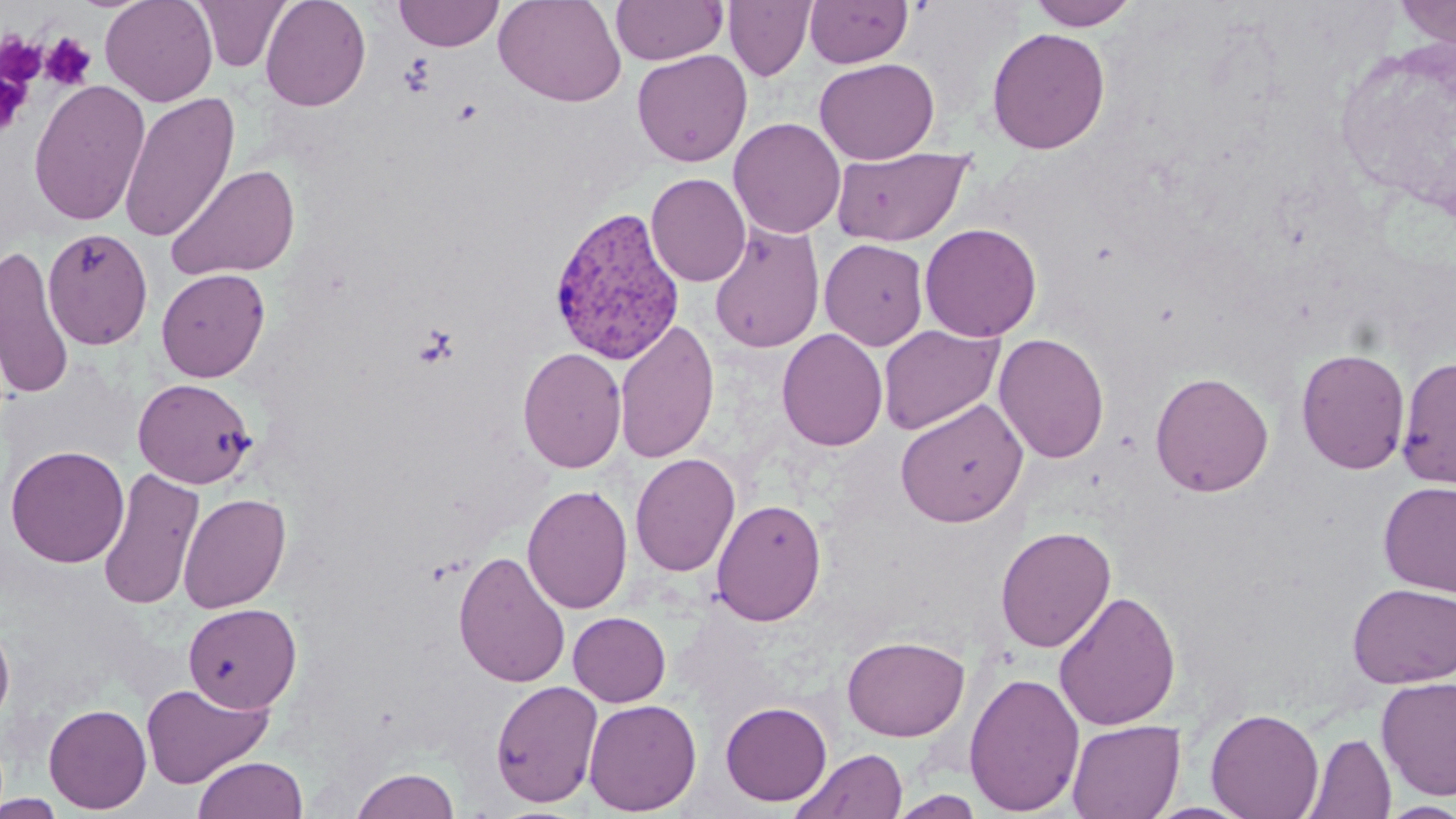
Summary:
  - Coordinate format: approximate bounding boxes as named x1/y1/x2/y2 corners in pixels
  - Platelet locations: (x1=0, y1=33, x2=46, y2=88), (x1=40, y1=33, x2=97, y2=91), (x1=0, y1=71, x2=31, y2=138)
  - Uninfected red blood cell locations: (x1=100, y1=0, x2=218, y2=107), (x1=192, y1=0, x2=290, y2=72), (x1=260, y1=0, x2=371, y2=111), (x1=393, y1=0, x2=505, y2=51), (x1=494, y1=0, x2=627, y2=107), (x1=610, y1=0, x2=727, y2=65), (x1=804, y1=0, x2=913, y2=68), (x1=1025, y1=0, x2=1141, y2=30), (x1=1392, y1=0, x2=1456, y2=47), (x1=723, y1=1, x2=816, y2=81), (x1=986, y1=27, x2=1111, y2=154), (x1=632, y1=49, x2=752, y2=167), (x1=814, y1=58, x2=939, y2=164), (x1=28, y1=79, x2=151, y2=227), (x1=119, y1=91, x2=239, y2=243), (x1=728, y1=117, x2=846, y2=239), (x1=831, y1=146, x2=972, y2=247), (x1=164, y1=163, x2=300, y2=282), (x1=645, y1=173, x2=751, y2=286), (x1=708, y1=222, x2=825, y2=353), (x1=919, y1=223, x2=1042, y2=341), (x1=42, y1=227, x2=153, y2=349), (x1=819, y1=238, x2=929, y2=351), (x1=0, y1=243, x2=75, y2=401), (x1=156, y1=268, x2=270, y2=381), (x1=614, y1=319, x2=719, y2=464), (x1=878, y1=324, x2=1004, y2=435), (x1=777, y1=328, x2=888, y2=451), (x1=993, y1=333, x2=1110, y2=464), (x1=517, y1=347, x2=627, y2=473), (x1=1296, y1=348, x2=1411, y2=474), (x1=1396, y1=356, x2=1456, y2=489), (x1=1150, y1=371, x2=1274, y2=497), (x1=133, y1=378, x2=256, y2=488), (x1=895, y1=398, x2=1028, y2=527), (x1=6, y1=444, x2=129, y2=568), (x1=629, y1=453, x2=740, y2=577), (x1=97, y1=467, x2=204, y2=610), (x1=1378, y1=481, x2=1456, y2=596), (x1=522, y1=484, x2=633, y2=615), (x1=177, y1=492, x2=291, y2=613), (x1=711, y1=498, x2=827, y2=626), (x1=995, y1=525, x2=1116, y2=653), (x1=453, y1=549, x2=571, y2=688), (x1=1347, y1=582, x2=1456, y2=688), (x1=1054, y1=589, x2=1182, y2=731), (x1=183, y1=602, x2=302, y2=713), (x1=568, y1=612, x2=670, y2=707), (x1=0, y1=617, x2=15, y2=728), (x1=841, y1=635, x2=970, y2=741), (x1=963, y1=670, x2=1085, y2=816), (x1=1376, y1=677, x2=1456, y2=800), (x1=490, y1=679, x2=603, y2=808), (x1=141, y1=682, x2=272, y2=788), (x1=583, y1=698, x2=702, y2=815), (x1=720, y1=701, x2=832, y2=806), (x1=44, y1=703, x2=152, y2=814), (x1=1205, y1=707, x2=1325, y2=819), (x1=1067, y1=719, x2=1184, y2=818), (x1=1303, y1=731, x2=1396, y2=819), (x1=791, y1=748, x2=908, y2=819), (x1=192, y1=756, x2=308, y2=818), (x1=351, y1=767, x2=460, y2=819), (x1=888, y1=791, x2=985, y2=818), (x1=1, y1=793, x2=67, y2=819), (x1=1141, y1=801, x2=1256, y2=818), (x1=1378, y1=801, x2=1456, y2=818)
  - Plasmodium vivax-infected red blood cell locations: (x1=547, y1=205, x2=686, y2=365)
  - Slide-level diagnosis: Plasmodium vivax
  - Magnification: 1000x
  - Modality: optical microscopy
  - Image size: 1456×819 pixels
  - Preparation: thin blood smear
  - Field of view: one of a larger specimen
  - Stain: May-Grünwald-Giemsa